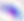
Summary:
  - Modality: micrograph
  - Magnification: 400x
  - Identification: Toxoplasma gondii